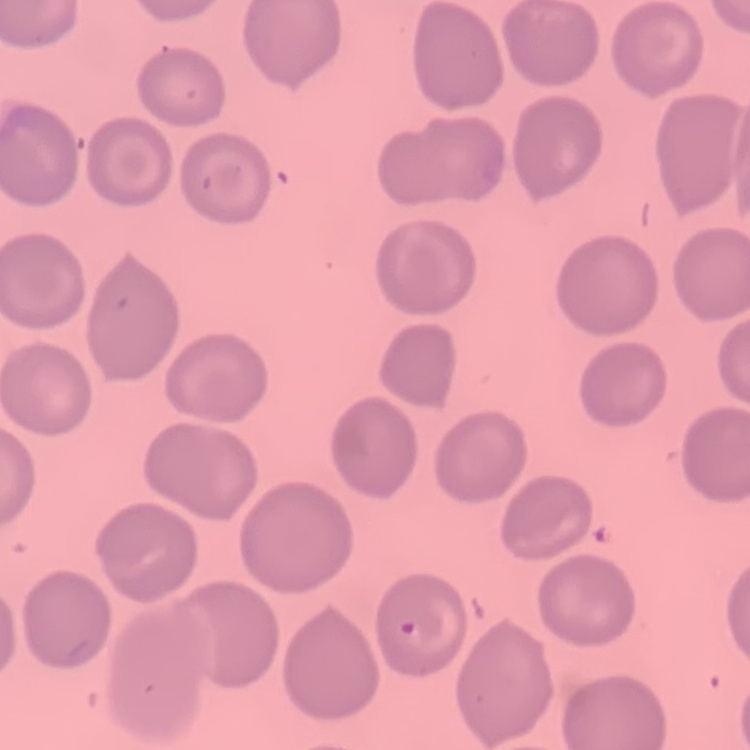

The red blood cells show no rouleaux formation. Square crop of a larger photomicrograph. Thin blood film. Field's or Giemsa stain.